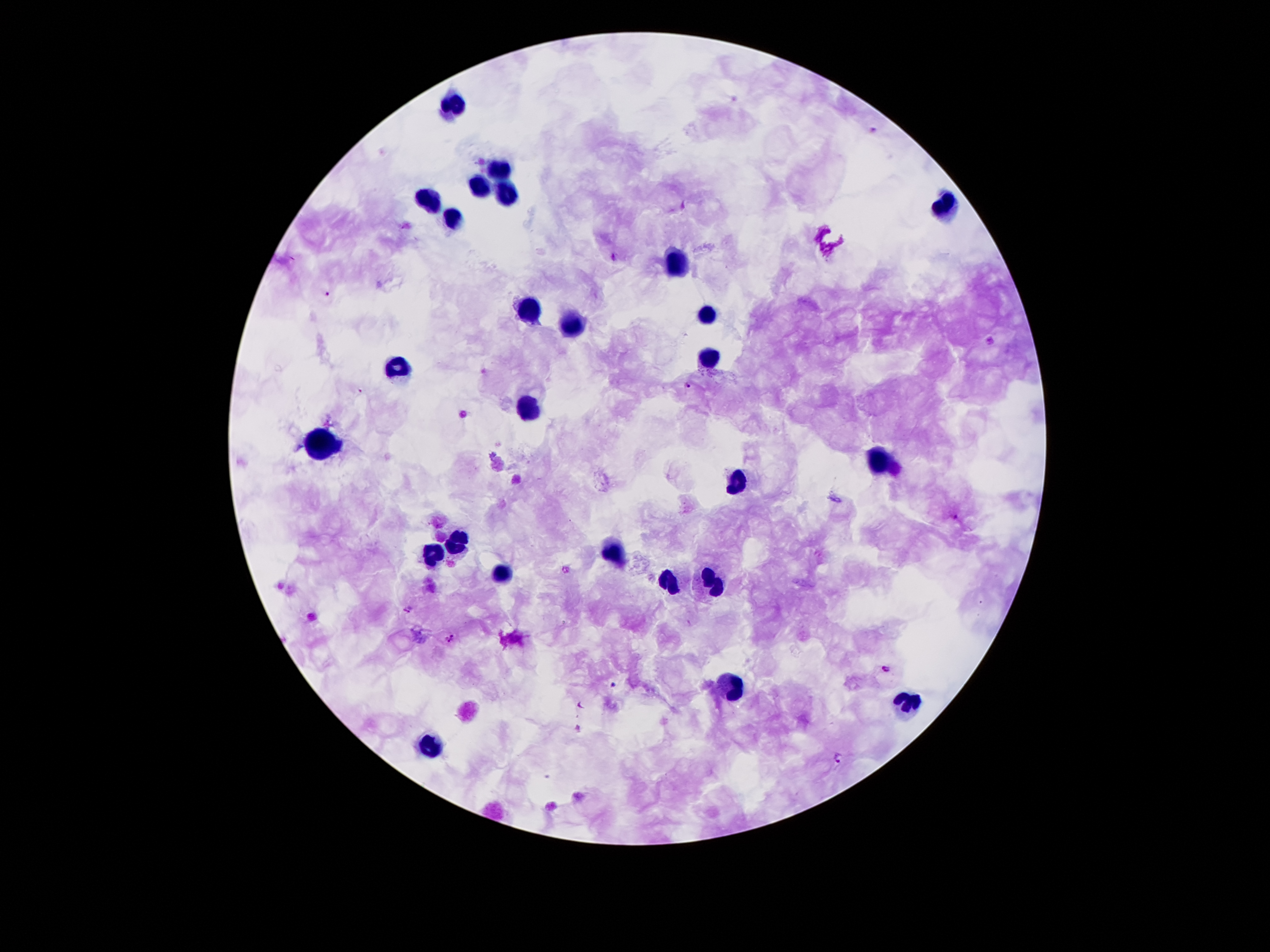

Smartphone photograph taken through the microscope eyepiece. One field from this slide. Patient malaria status: infected with Plasmodium falciparum. Image is 1270×952 pixels. Giemsa-stained preparation. 100x magnification. Thick peripheral-blood smear.